Assess this cell for malaria.
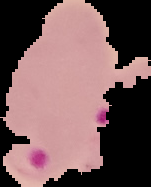
Parasitized.

Image is 151×187 pixels. From a thin blood smear. Segmented cell region on a black background.